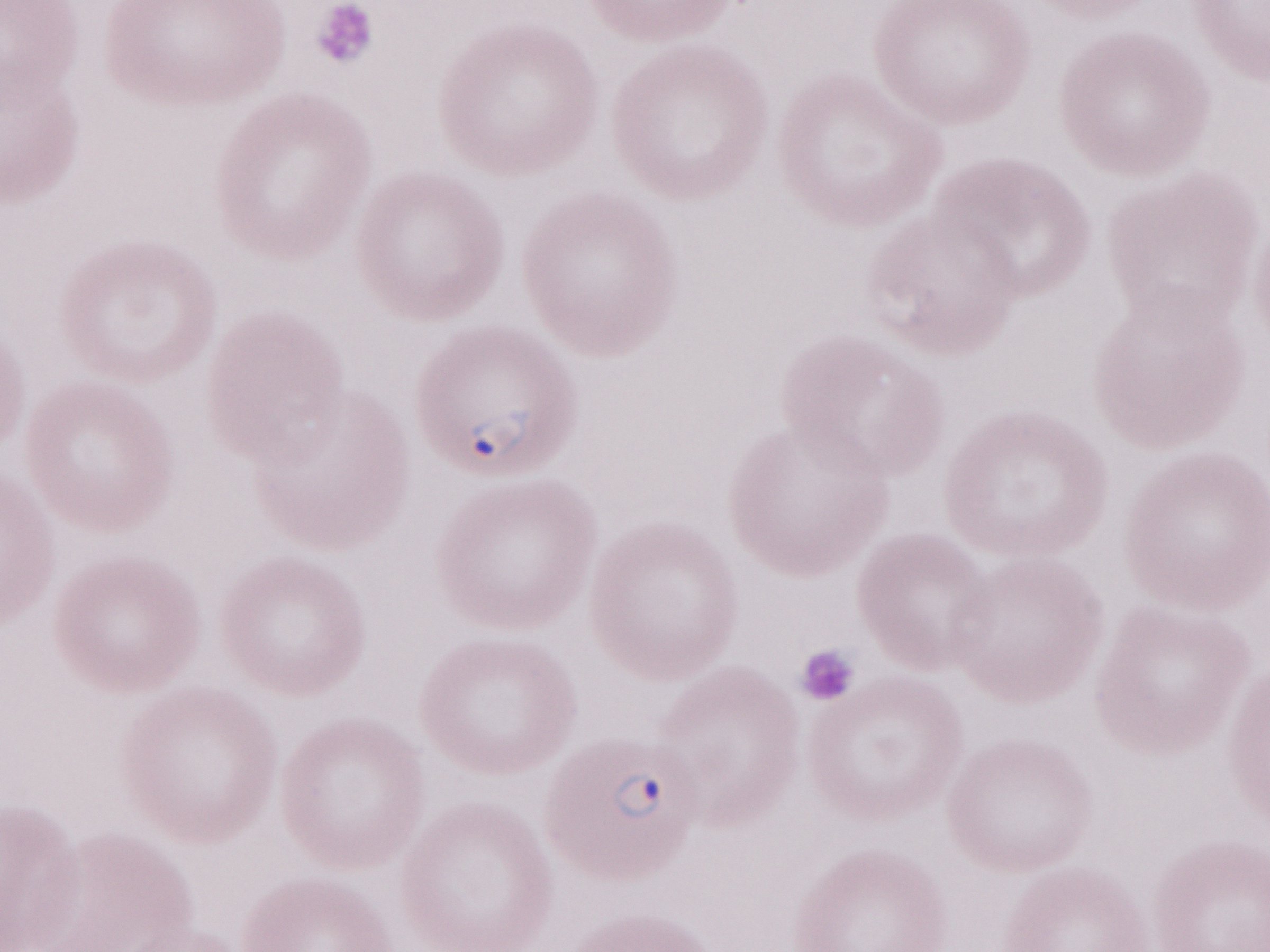
Patient-level malaria diagnosis: positive. Single field of view. May-Grünwald-Giemsa (MGG) stain. Magnification: 1,000x. Olympus BX43 microscope, Olympus DP73 camera. Thin peripheral-blood smear. Image is 1270×952 pixels.